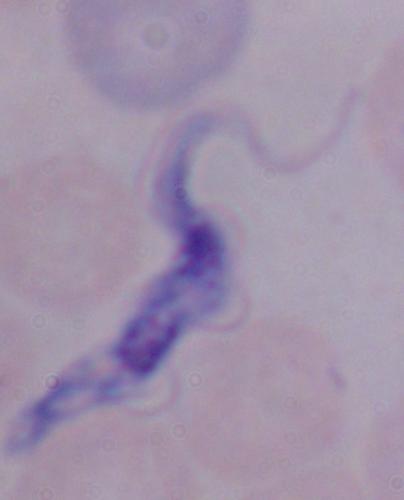
Summary:
  - Modality: photomicrograph
  - Magnification: 1000x
  - Identification: trypanosome